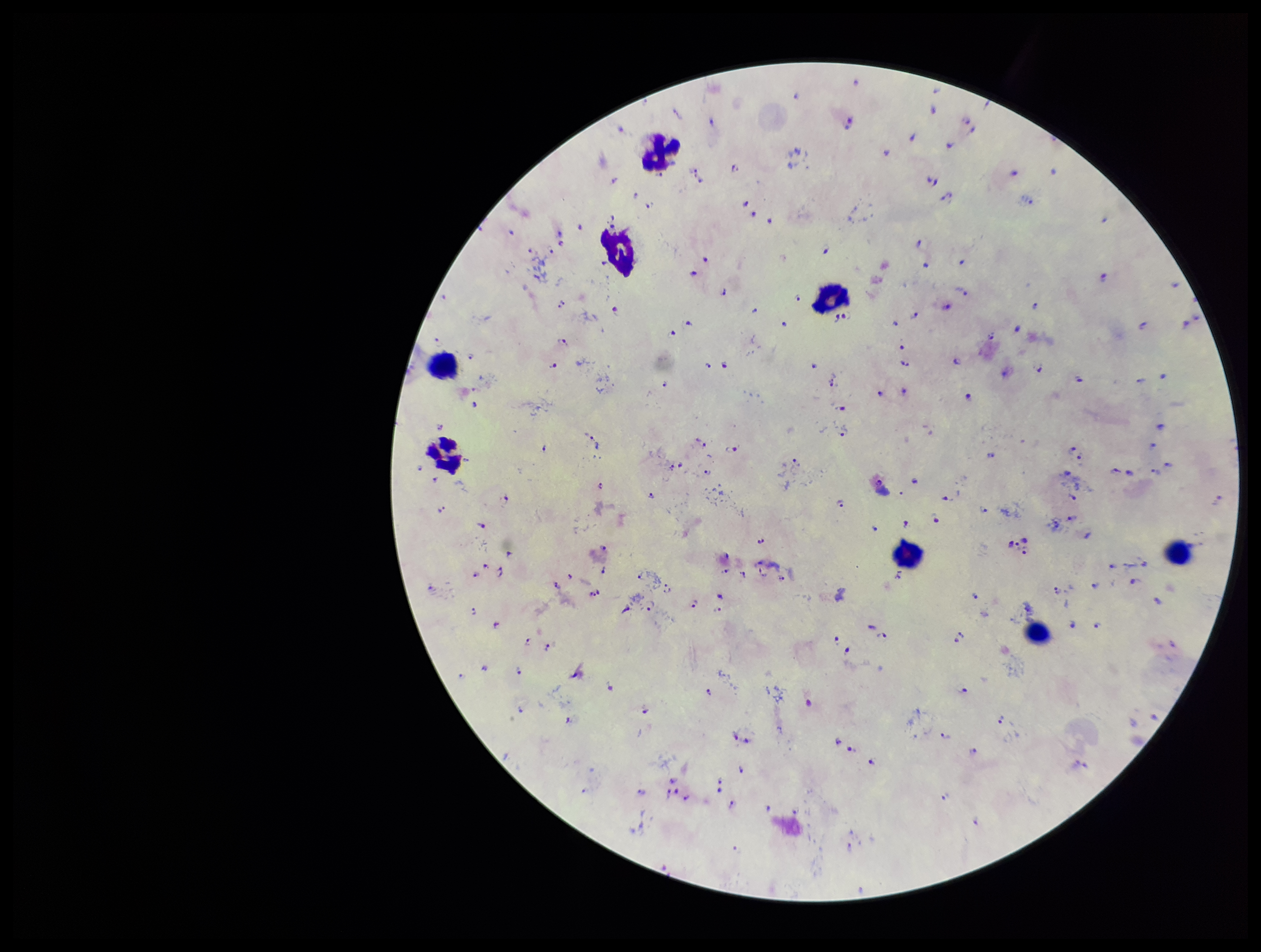

parasite_count: 169
preparation: thick smear
species_reported_for_this_patient: Plasmodium falciparum
leukocyte_count: 8
image_size: 1261×952 pixels
capture: smartphone photograph through the microscope eyepiece
plasmodium_parasites: detected
stain: Giemsa
patient_malaria_status: infected
field_of_view: single